Assess this cell for malaria.
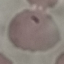

It is parasitized.

preparation: thin smear
capture: smartphone camera at the microscope eyepiece
image_type: automatically extracted cell patch, resized to 64 × 64 pixels
stain: Giemsa